Identify the parasite.
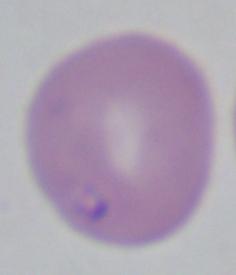

Babesia.

Captured at 1000x magnification. Micrograph.